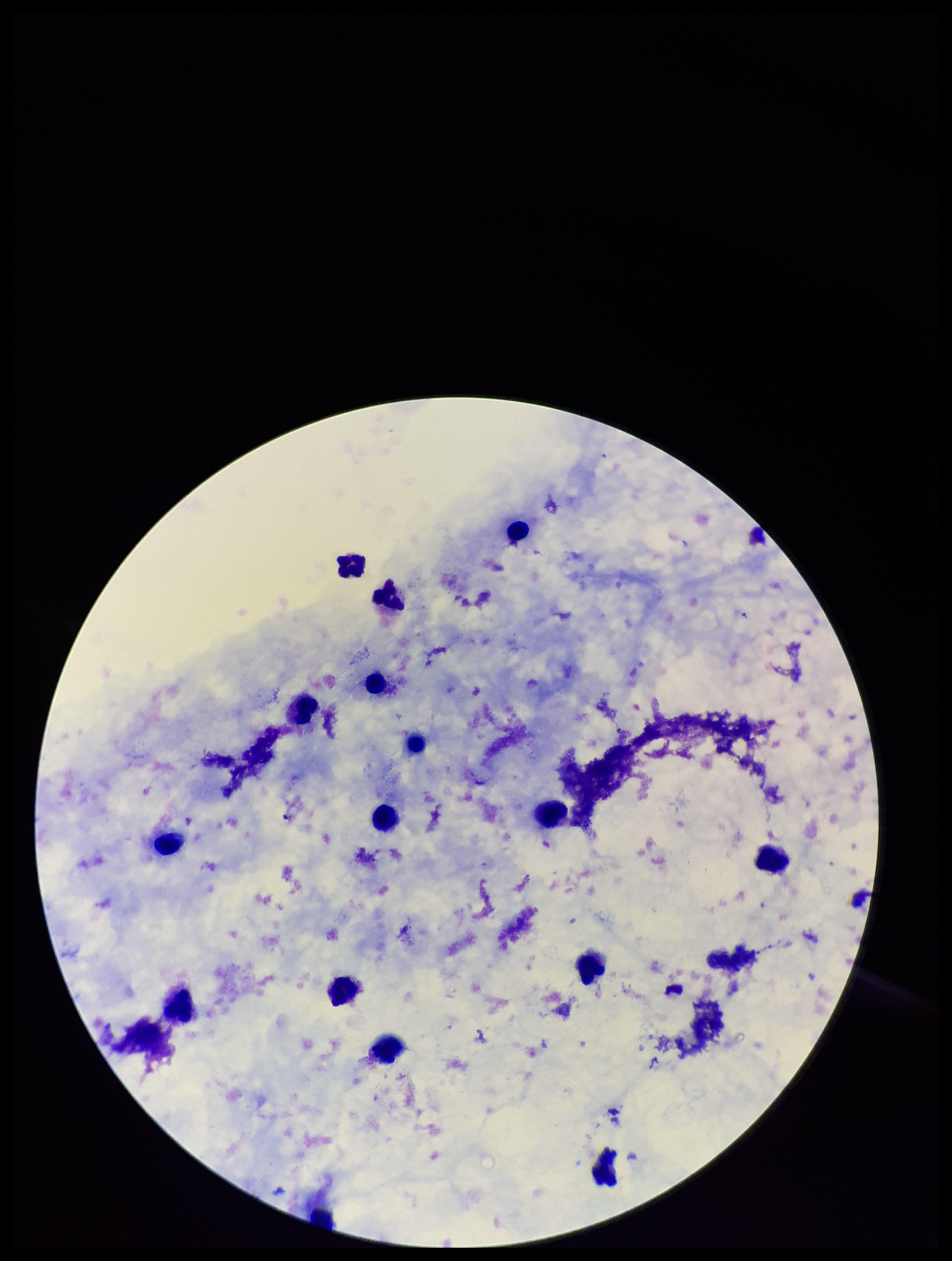

capture: smartphone photograph through the microscope eyepiece
leukocyte_count: 15
patient_malaria_status: negative
stain: Giemsa
plasmodium_parasites: none seen
preparation: thick
image_size: 952×1261 pixels
parasite_count: 0
field_of_view: single